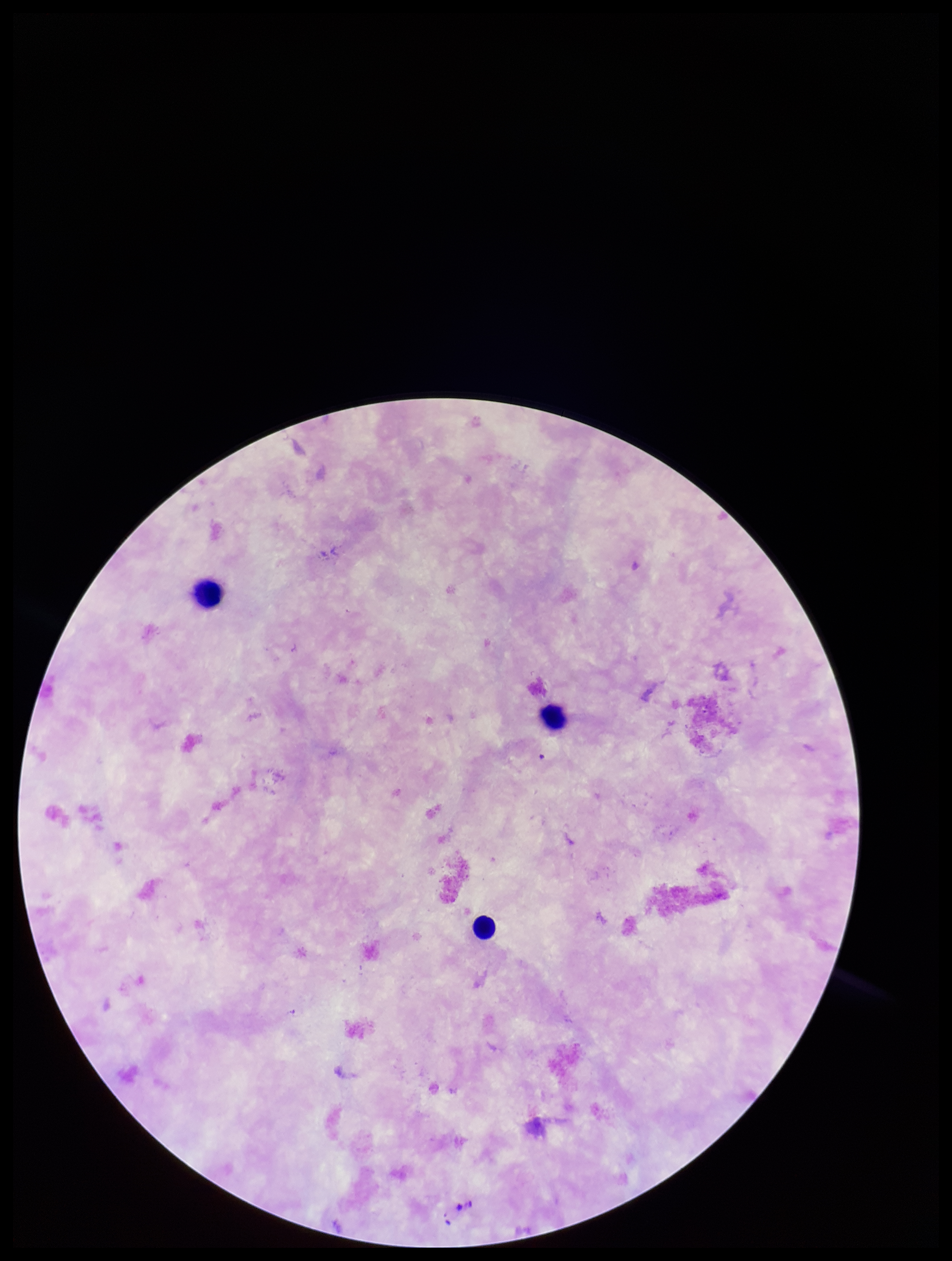

patient_malaria_status: negative
plasmodium_parasites: none seen
stain: Giemsa
capture: smartphone photograph through the microscope eyepiece
field_of_view: single
parasite_count: 0
leukocyte_count: 3
image_size: 952×1261 pixels
preparation: thick smear